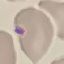

malaria status = uninfected
stain = Giemsa
image type = automatically extracted cell patch, resized to 64 × 64 pixels
preparation = thin blood smear
capture = smartphone camera at the microscope eyepiece